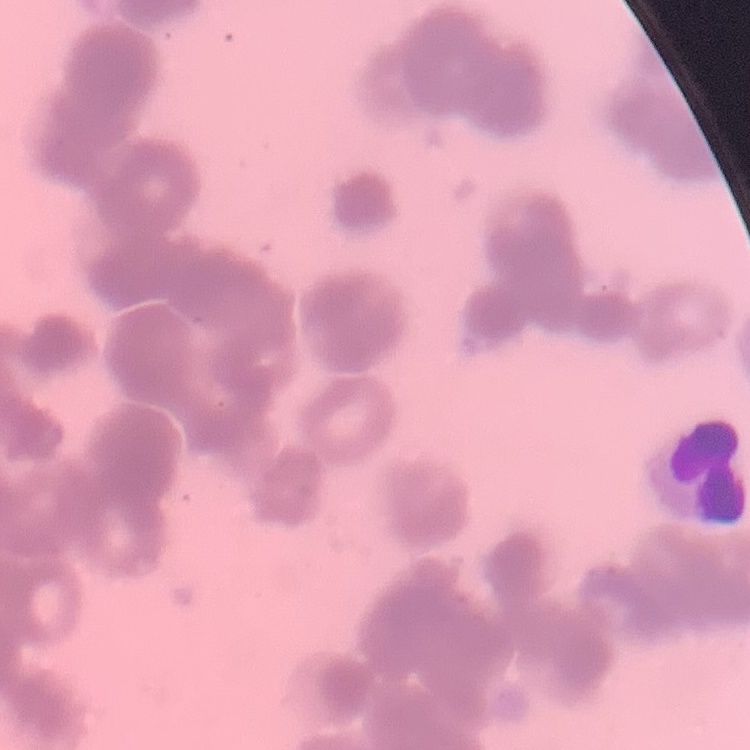

The erythrocytes exhibit rouleaux formation. Square crop of a larger photomicrograph. Field's or Giemsa stain. Thin blood film.